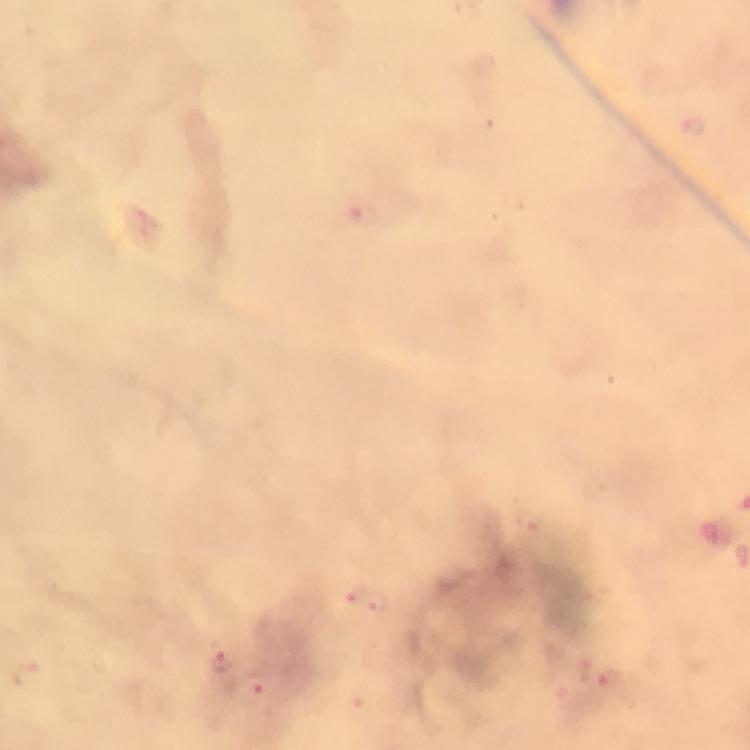
capture = smartphone photograph through a microscope
magnification = 100x
Plasmodium parasite locations = approximate centers as {x, y} in pixels: {693, 126}, {363, 212}, {370, 601}, {221, 659}, {27, 672}, {608, 683}, {253, 691}, {361, 706}
stain = Giemsa
immersion oil = applied
cropped from = one field of view
context = from a diagnostic examination for malaria
preparation = thick smear
image size = 750×750 pixels